Assess the morphology of the erythrocytes.
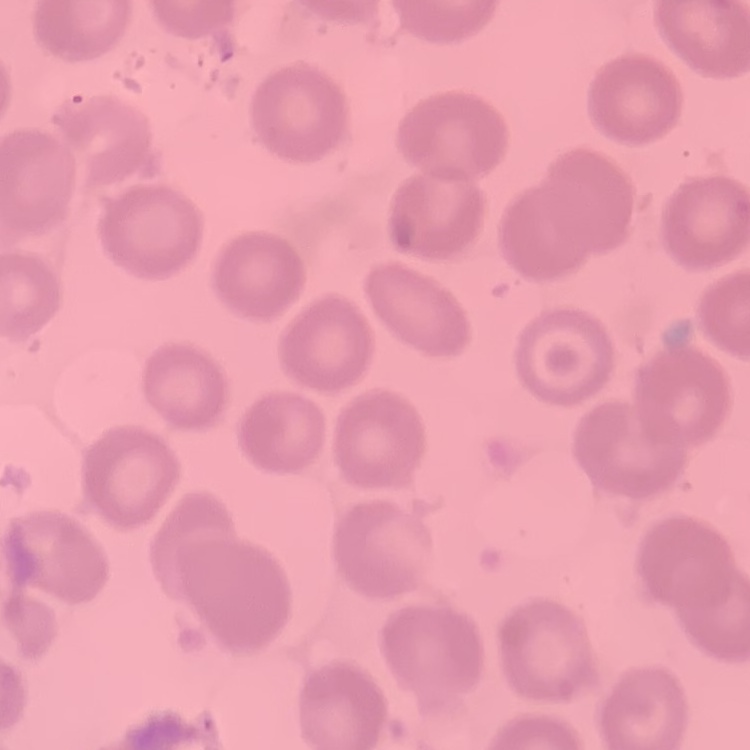

No rouleaux formation.

Summary:
  - Image type: one tile cut from a larger photomicrograph
  - Stain: Field's or Giemsa
  - Preparation: thin peripheral smear